State the blood parasite species.
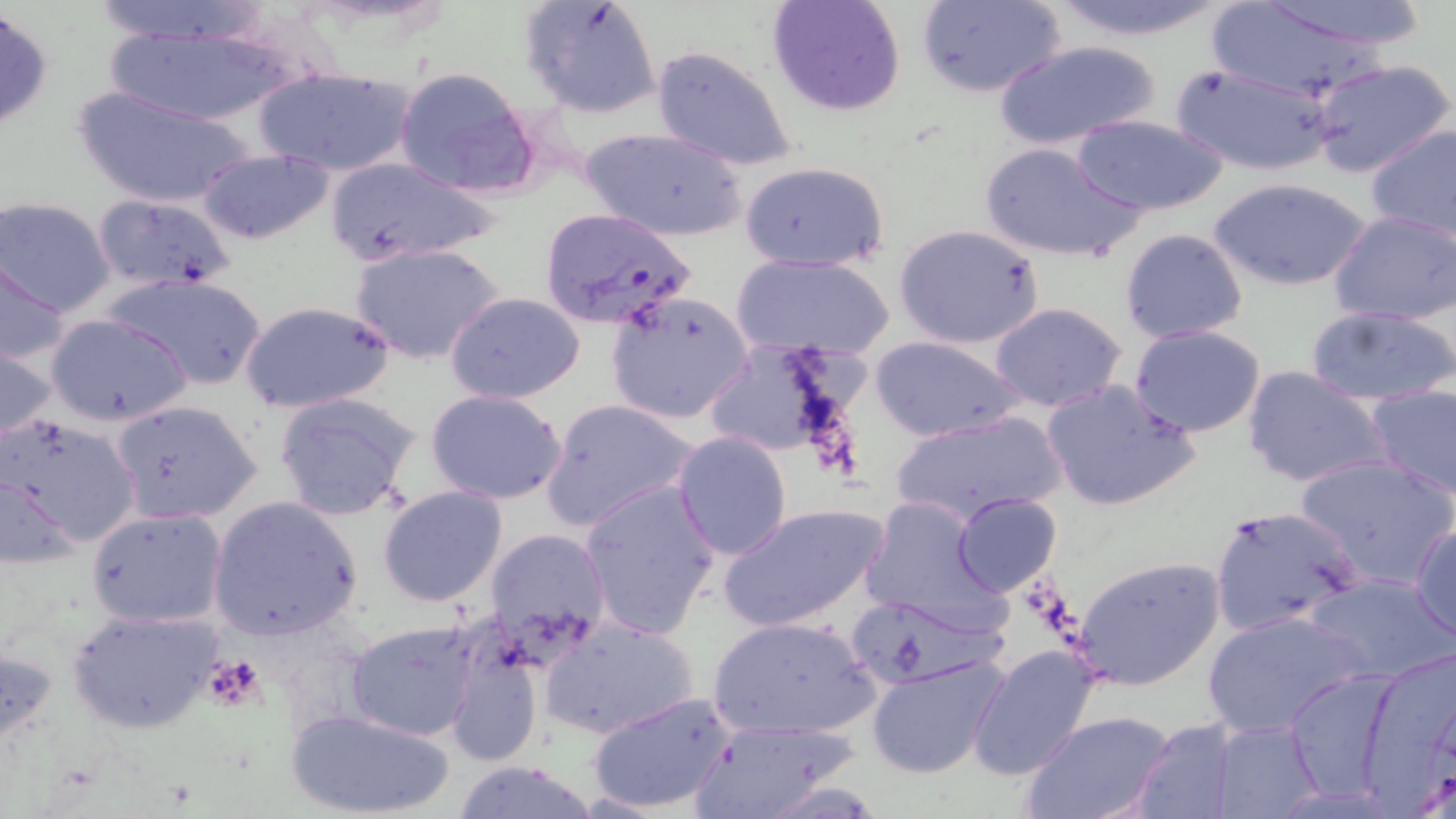
Plasmodium falciparum.

platelet locations = approximate bounding boxes as (x1,y1)-(x2,y2) corner pairs in pixels: (203,657)-(267,710)
image size = 1456×819 pixels
Plasmodium falciparum-infected red blood cell locations = approximate bounding boxes as (x1,y1)-(x2,y2) corner pairs in pixels: (539,207)-(698,331)
preparation = thin blood film
uninfected red blood cell locations = approximate bounding boxes as (x1,y1)-(x2,y2) corner pairs in pixels: (85,0)-(278,47), (766,0)-(908,117), (917,0)-(1067,99), (1048,0)-(1233,42), (1247,0)-(1426,52), (1205,1)-(1402,105), (518,2)-(660,120), (100,20)-(296,127), (992,39)-(1162,152), (649,44)-(801,173), (1307,58)-(1454,179), (1168,60)-(1337,177), (252,65)-(420,180), (393,66)-(541,200), (74,84)-(262,208), (1069,115)-(1228,216), (1365,125)-(1456,242), (579,126)-(749,243), (978,140)-(1144,265), (196,149)-(335,245), (325,157)-(501,266), (738,160)-(889,272), (1210,177)-(1372,293), (92,191)-(238,294), (2,196)-(117,317), (1328,211)-(1456,325), (894,224)-(1046,350), (1120,228)-(1249,345), (350,242)-(506,366), (731,252)-(895,361), (1,258)-(71,367), (103,271)-(269,391), (444,292)-(588,404), (605,292)-(755,426), (239,301)-(394,412), (989,302)-(1127,413), (1305,305)-(1456,408), (43,311)-(194,427), (1128,325)-(1269,437), (870,336)-(1026,442), (0,337)-(61,452), (699,337)-(873,471), (1242,365)-(1389,490), (1039,379)-(1201,511), (1362,381)-(1456,500), (425,388)-(568,504), (273,391)-(419,522), (540,397)-(699,534), (111,399)-(264,526), (889,408)-(1068,529), (0,412)-(143,549), (673,431)-(792,560), (1294,452)-(1456,591), (0,473)-(83,573), (578,479)-(721,640), (377,485)-(509,607), (952,493)-(1061,595), (859,494)-(1010,632), (207,497)-(363,640), (717,501)-(890,633), (1207,503)-(1365,639), (85,508)-(228,629), (1410,523)-(1456,641), (481,525)-(613,661), (1071,555)-(1226,690), (1301,572)-(1453,682), (65,605)-(223,736), (1200,608)-(1370,740), (707,615)-(879,742), (540,616)-(699,740), (346,619)-(480,740), (439,625)-(547,769), (1359,643)-(1456,804), (967,644)-(1102,780), (865,653)-(1009,781), (1285,670)-(1399,802), (586,691)-(739,815), (285,708)-(457,818), (1024,710)-(1175,819), (685,718)-(858,819), (1130,719)-(1242,819), (1211,719)-(1325,818), (450,759)-(603,819)
stain = May-Grünwald-Giemsa
magnification = 1000x
field of view = single
modality = optical microscopy